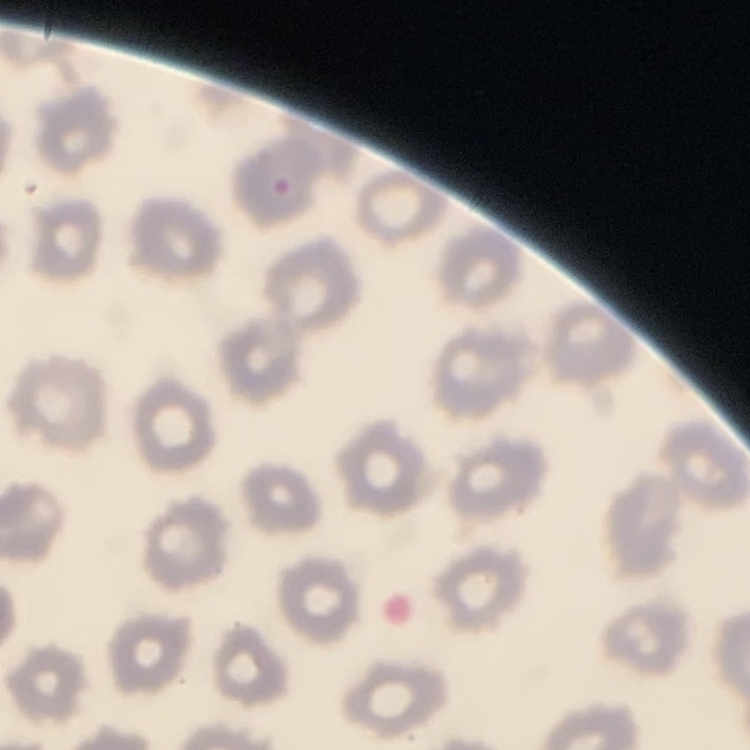
The erythrocytes exhibit no rouleaux formation. Thin blood film. Stained with either Field's or Giemsa. Square crop of a larger photomicrograph.